Report the malaria status.
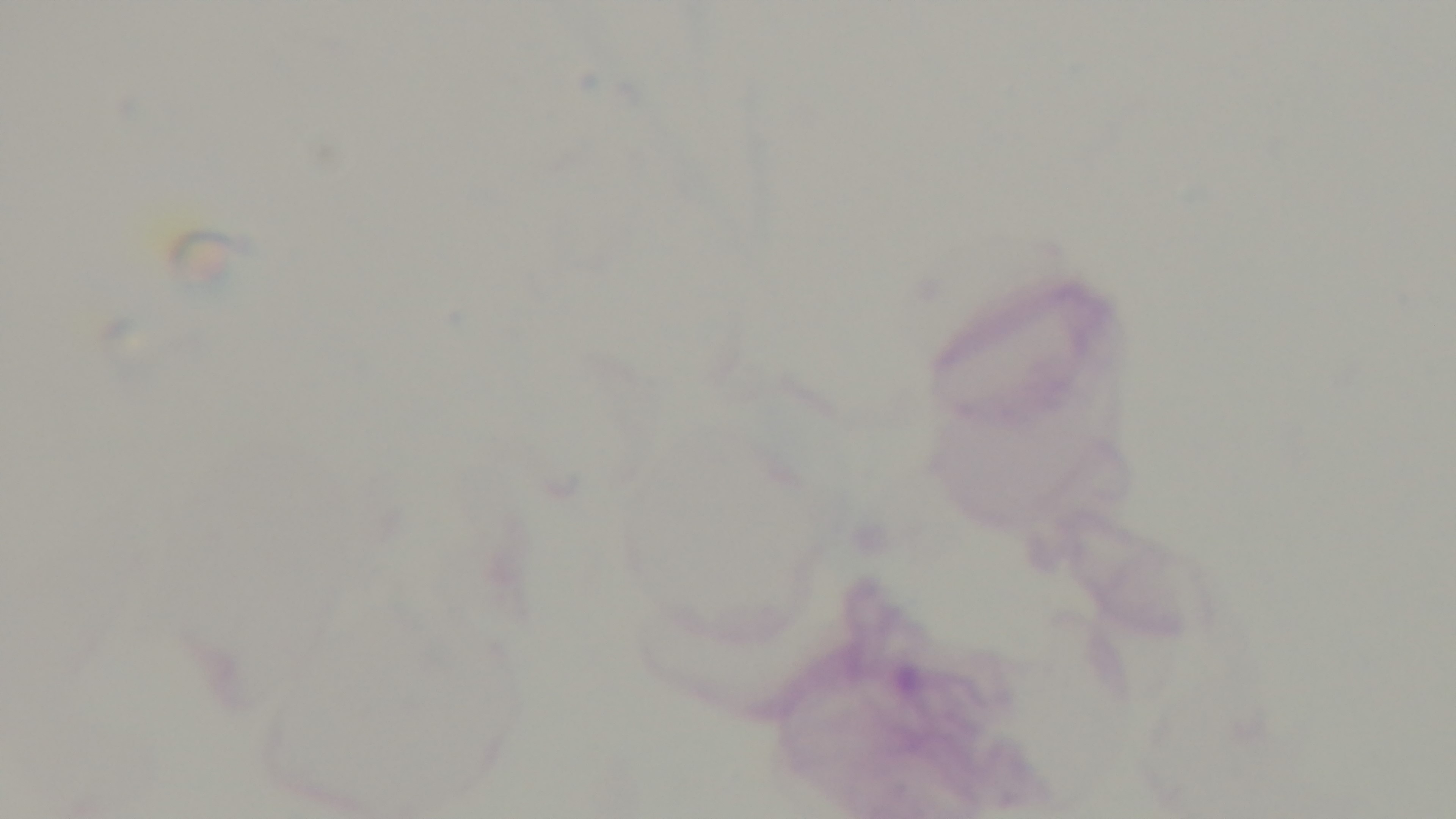

Negative.

Light microscopy. Oil-immersion objective, 100x. Mounted 4K digital camera. One field from the slide. Giemsa stain. Preparation: thick blood film.